State the preparation type.
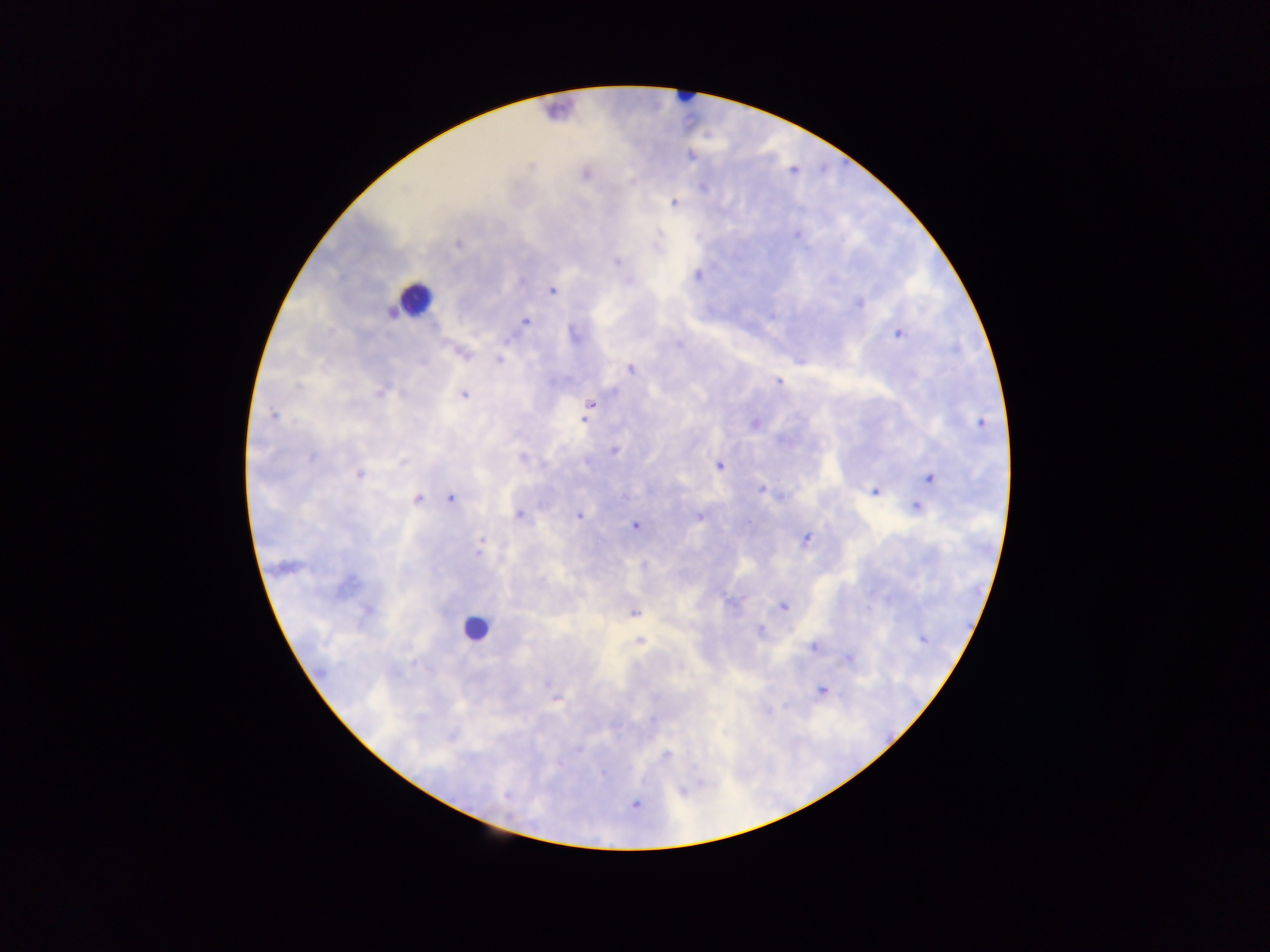
Thick blood film.

Approximate centers as [x, y] in pixels. Leukocyte locations: [685, 95], [558, 110], [414, 298], [475, 628]. Malaria parasite locations: [585, 174], [674, 202], [796, 234], [458, 243], [616, 261], [551, 290], [859, 304], [392, 311], [525, 321], [898, 333], [574, 334], [461, 352], [499, 361], [630, 369], [778, 381], [380, 390], [463, 395], [589, 405], [272, 415], [755, 423], [979, 423], [614, 451], [718, 465], [359, 474], [929, 478], [762, 488], [875, 491], [451, 496], [417, 498], [917, 506], [518, 514], [579, 515], [699, 517], [635, 525], [806, 539], [285, 566], [783, 606], [633, 611], [759, 630], [923, 639], [640, 641], [813, 645], [849, 659], [821, 691], [555, 696], [666, 755], [634, 803]. Mobile-phone photograph taken through the microscope. Sample from Ghana. Image is 1270×952 pixels. One field of view.